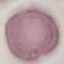

Summary:
  - Malaria status: uninfected
  - Stain: Giemsa
  - Preparation: thin blood film
  - Image type: automatically extracted cell patch, resized to 64 × 64 pixels
  - Capture: smartphone through the microscope eyepiece